Locate every Plasmodium falciparum-infected red blood cell.
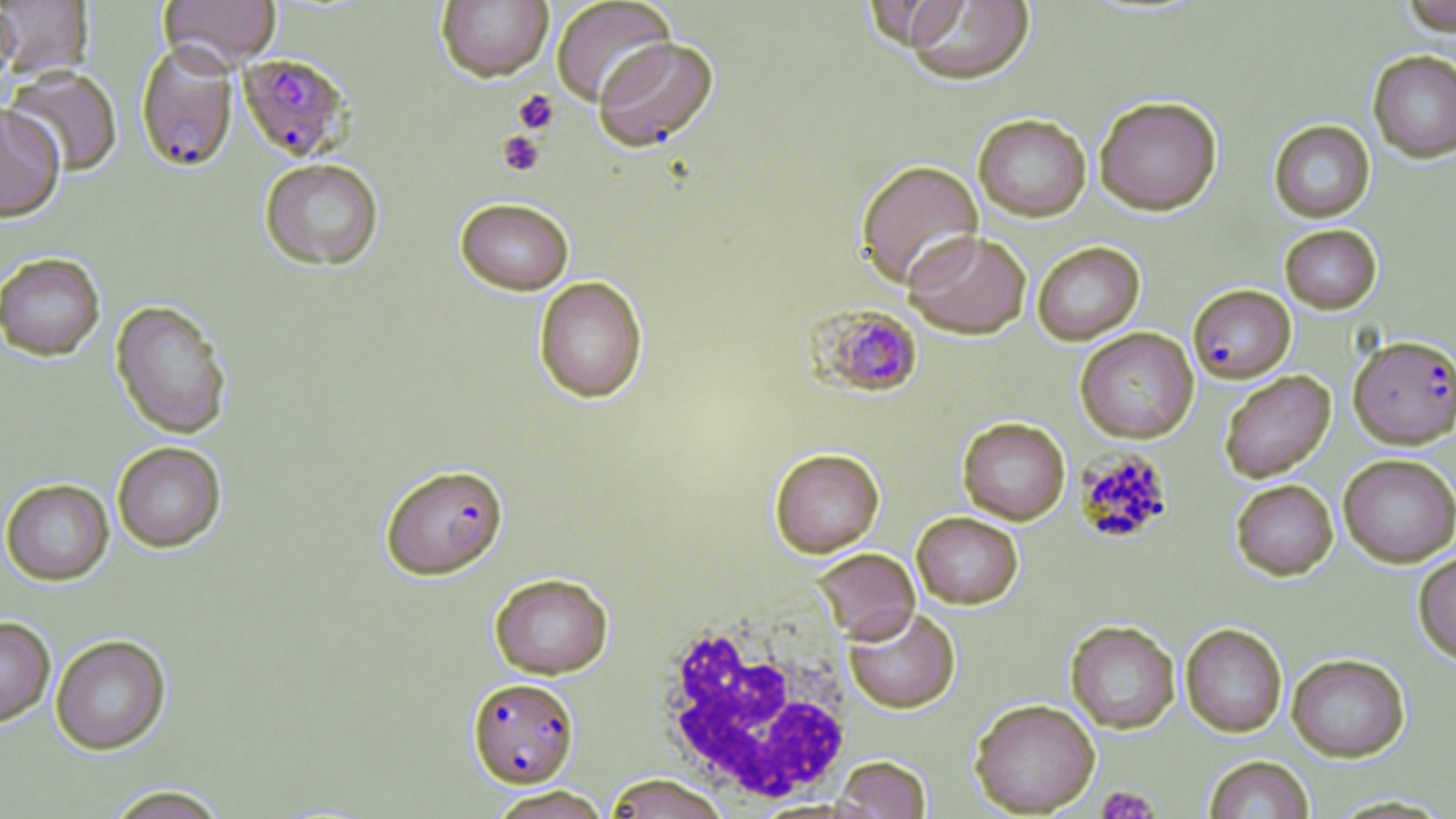
Approximate bounding boxes as (x1,y1)-(x2,y2) corner pairs in pixels.
Plasmodium falciparum-infected red blood cells: (135,41)-(239,172), (238,53)-(352,161), (1188,284)-(1295,382), (810,304)-(924,399), (1349,335)-(1456,449), (1076,448)-(1173,544), (380,463)-(508,580), (467,677)-(579,788).

White blood cell locations: (650,608)-(858,806). Platelet locations: (513,89)-(559,134), (497,131)-(545,177), (1097,786)-(1160,818). Uninfected red blood cell locations: (158,0)-(280,72), (436,0)-(553,82), (551,0)-(676,107), (895,0)-(1036,85), (0,1)-(93,80), (1402,1)-(1456,35), (0,3)-(20,94), (593,36)-(718,151), (1368,50)-(1456,162), (4,67)-(123,177), (1094,95)-(1222,215), (0,103)-(65,222), (973,113)-(1092,221), (1269,120)-(1375,222), (259,158)-(384,271), (855,159)-(984,290), (455,197)-(574,294), (1280,224)-(1382,313), (903,230)-(1031,339), (1032,241)-(1145,345), (0,252)-(105,361), (533,276)-(648,403), (111,300)-(232,439), (1075,327)-(1198,443), (1219,370)-(1335,483), (957,417)-(1070,524), (112,442)-(226,552), (770,447)-(884,557), (1338,453)-(1456,567), (2,479)-(114,585), (1230,479)-(1338,580), (912,511)-(1023,608), (812,547)-(920,643), (1413,549)-(1456,666), (489,573)-(613,678), (844,606)-(960,713), (0,616)-(56,727), (1066,620)-(1180,734), (1181,623)-(1286,737), (51,635)-(170,754), (1287,653)-(1410,761), (970,699)-(1100,817), (833,755)-(931,818), (1204,755)-(1314,818), (605,773)-(730,819), (103,785)-(229,818), (487,786)-(612,818). Slide-level diagnosis: Plasmodium falciparum. May-Grünwald-Giemsa-stained preparation. Thin blood smear. Captured at 1000x magnification. Light microscopy. Image is 1456×819 pixels. One field of a larger specimen.